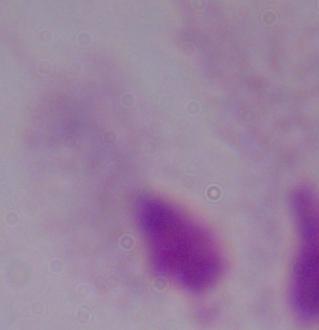
Summary:
  - Magnification: 1000x
  - Modality: micrograph
  - Identification: trichomonad